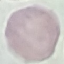
Result: no malaria parasites seen. Giemsa stain. Cell patch, automatically extracted from a larger field of view and resized to 64 × 64 pixels. Acquired by smartphone through the microscope eyepiece. Thin blood film.